Give the extent of all uninfected red blood cells.
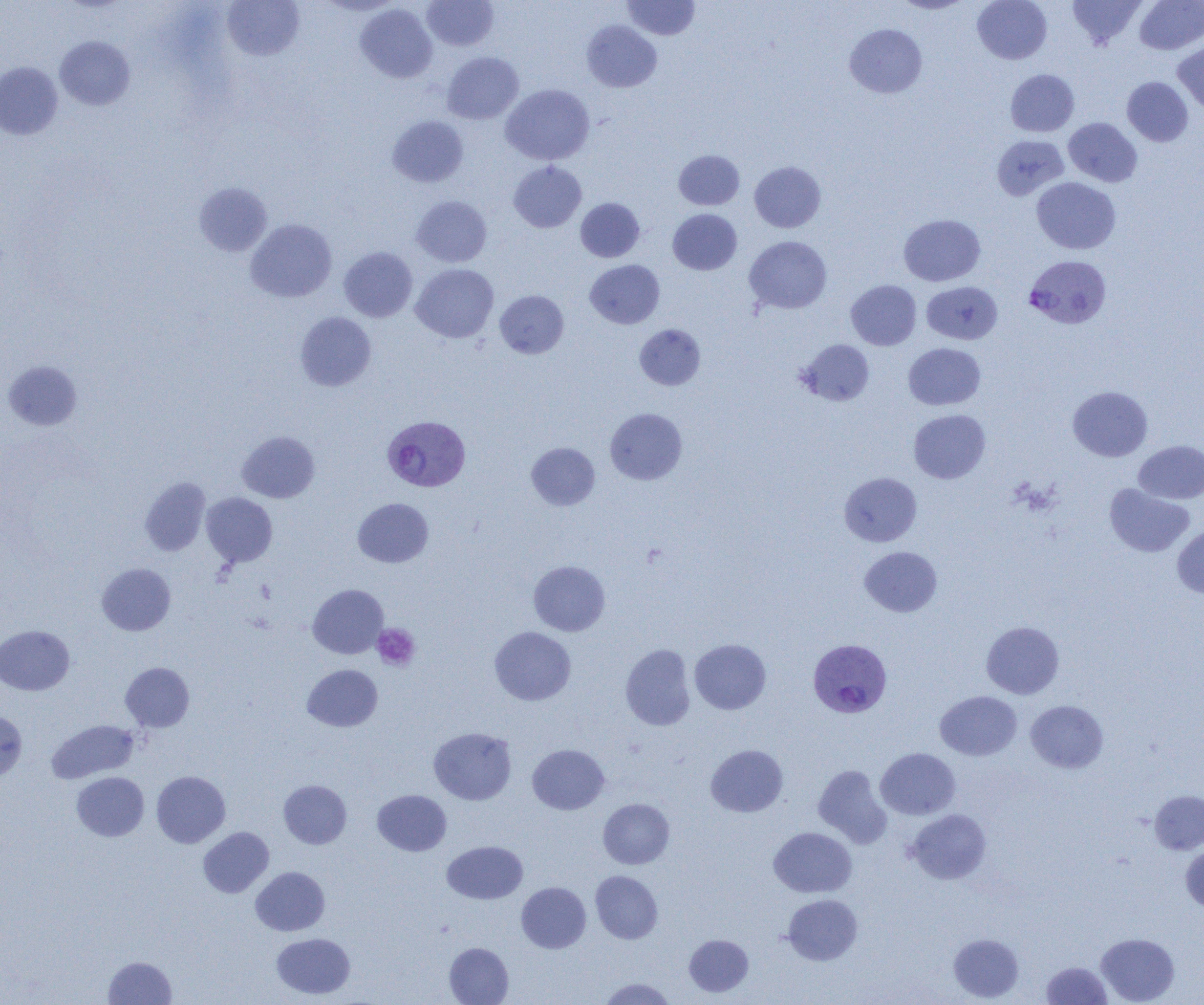

Approximate bounding boxes as [x1, y1, x2, y2] in pixels.
Uninfected red blood cells: [422, 0, 498, 50], [622, 0, 699, 40], [892, 0, 973, 14], [972, 0, 1052, 64], [1068, 0, 1146, 48], [1135, 0, 1204, 54], [222, 1, 304, 61], [317, 1, 402, 15], [355, 4, 437, 83], [582, 20, 662, 92], [844, 23, 927, 98], [55, 36, 135, 110], [1173, 40, 1204, 114], [442, 52, 523, 124], [0, 62, 63, 139], [1006, 69, 1079, 136], [1122, 76, 1193, 146], [501, 84, 594, 165], [387, 115, 468, 187], [1064, 118, 1142, 187], [991, 135, 1069, 200], [674, 150, 744, 210], [508, 161, 586, 232], [749, 161, 825, 232], [1032, 177, 1120, 254], [194, 182, 272, 256], [411, 195, 491, 266], [576, 198, 644, 262], [668, 209, 742, 274], [899, 214, 985, 286], [245, 219, 336, 302], [744, 236, 832, 314], [339, 247, 417, 322], [585, 260, 664, 328], [411, 263, 498, 343], [846, 280, 921, 350], [922, 281, 1002, 344], [495, 290, 569, 358], [296, 312, 376, 391], [635, 324, 705, 390], [796, 339, 874, 406], [903, 343, 986, 410], [3, 360, 82, 431], [1067, 386, 1153, 461], [605, 408, 687, 484], [909, 409, 990, 483], [237, 431, 320, 503], [1134, 440, 1204, 504], [526, 442, 600, 510], [839, 472, 922, 546], [140, 477, 211, 556], [1105, 483, 1193, 557], [201, 493, 277, 567], [353, 498, 433, 568], [1172, 526, 1204, 597], [859, 546, 942, 617], [529, 560, 610, 636], [97, 563, 175, 635], [308, 584, 388, 658], [982, 621, 1064, 699], [0, 625, 74, 695], [490, 626, 576, 705], [690, 638, 771, 714], [620, 644, 695, 730], [121, 662, 194, 731], [302, 664, 382, 731], [935, 691, 1021, 760], [1026, 700, 1108, 773], [0, 711, 27, 782], [46, 719, 139, 783], [429, 727, 516, 805], [527, 744, 609, 814], [706, 744, 788, 817], [876, 748, 960, 819], [813, 764, 891, 848], [151, 771, 230, 848], [72, 772, 149, 841], [279, 780, 351, 849], [373, 790, 451, 856], [1150, 790, 1204, 854], [598, 798, 674, 868], [907, 809, 991, 884], [198, 827, 274, 897], [769, 827, 857, 897], [442, 841, 528, 904], [1181, 844, 1204, 913], [251, 866, 329, 936], [590, 871, 663, 944], [517, 882, 591, 953], [782, 894, 863, 965], [271, 933, 355, 999], [948, 933, 1024, 1002], [1096, 933, 1179, 1004], [684, 934, 753, 997], [445, 942, 513, 1004], [103, 956, 176, 1004], [1041, 961, 1111, 1004], [598, 977, 676, 1004].

Summary:
  - Platelet locations: [373, 624, 420, 670]
  - Plasmodium vivax-infected red blood cell locations: [1024, 255, 1112, 329], [382, 417, 470, 493], [808, 638, 891, 717]
  - Slide-level diagnosis: Plasmodium vivax
  - Modality: optical microscopy
  - Magnification: 1000x
  - Image size: 1204×1005 pixels
  - Field of view: single
  - Preparation: thin blood smear